Locate the cells, classifying each as a parasitized RBC, an uninfected RBC, or a WBC.
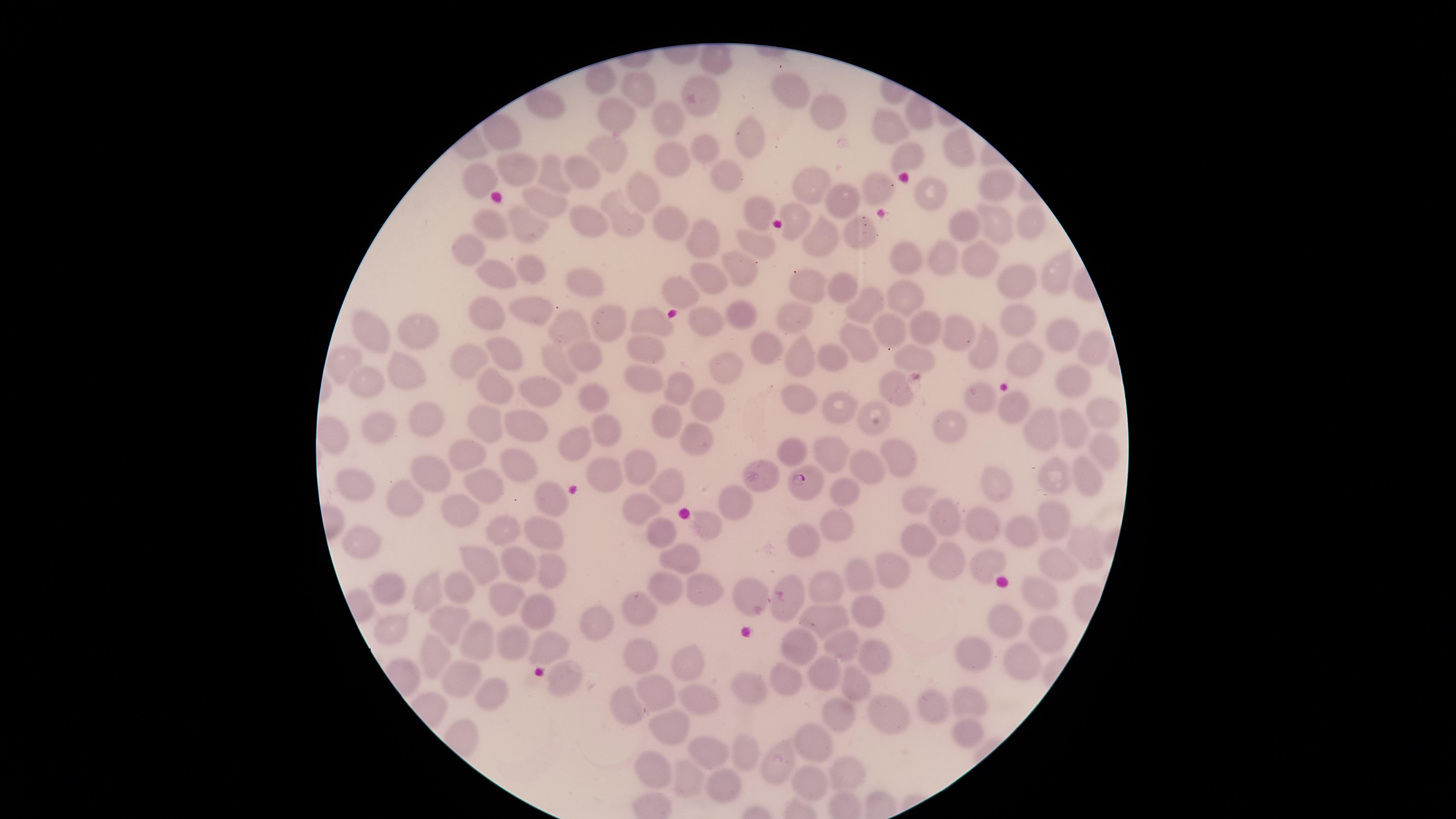
Approximate marker points, in pixels from the top-left corner.
Parasitized RBCs: (x=807, y=483).
Uninfected RBCs: (x=713, y=52), (x=605, y=78), (x=638, y=85), (x=795, y=90), (x=703, y=100), (x=547, y=107), (x=824, y=114), (x=913, y=114), (x=620, y=115), (x=673, y=118), (x=890, y=129), (x=748, y=133), (x=504, y=135), (x=705, y=145), (x=960, y=146), (x=603, y=151), (x=913, y=154), (x=671, y=158), (x=582, y=168), (x=726, y=172), (x=552, y=173), (x=511, y=177), (x=809, y=180), (x=999, y=184), (x=477, y=185), (x=639, y=185), (x=880, y=188), (x=929, y=197), (x=544, y=198), (x=843, y=199), (x=758, y=204), (x=622, y=215), (x=489, y=222), (x=598, y=222), (x=667, y=222), (x=1026, y=224), (x=994, y=225), (x=794, y=226), (x=855, y=226), (x=971, y=226), (x=530, y=227), (x=700, y=235), (x=754, y=236), (x=814, y=238), (x=471, y=248), (x=941, y=251), (x=898, y=255), (x=975, y=256), (x=742, y=266), (x=525, y=269), (x=494, y=270), (x=1054, y=270), (x=707, y=275), (x=1007, y=281), (x=581, y=284), (x=674, y=285), (x=807, y=285), (x=841, y=288), (x=909, y=294), (x=869, y=306), (x=526, y=309), (x=746, y=312), (x=487, y=313), (x=797, y=314), (x=704, y=316), (x=649, y=317), (x=1013, y=317), (x=606, y=321), (x=563, y=324), (x=429, y=327), (x=920, y=327), (x=959, y=329), (x=1060, y=329), (x=375, y=332), (x=892, y=332), (x=1089, y=341), (x=862, y=342), (x=643, y=345), (x=761, y=345), (x=987, y=351), (x=501, y=353), (x=583, y=355), (x=913, y=355), (x=806, y=356), (x=830, y=356), (x=339, y=360), (x=1025, y=360), (x=563, y=363), (x=476, y=365), (x=725, y=365), (x=410, y=372), (x=646, y=377), (x=1075, y=377), (x=371, y=378), (x=543, y=387), (x=496, y=389), (x=674, y=389), (x=899, y=389), (x=589, y=392), (x=981, y=395), (x=800, y=397), (x=706, y=401), (x=1012, y=407), (x=839, y=411), (x=1101, y=413), (x=421, y=418), (x=672, y=418), (x=481, y=419), (x=866, y=421), (x=951, y=421), (x=516, y=424), (x=1075, y=426), (x=601, y=428), (x=381, y=430), (x=1048, y=430), (x=335, y=436), (x=696, y=436), (x=459, y=447), (x=574, y=447), (x=836, y=449), (x=1106, y=450), (x=790, y=452), (x=895, y=454), (x=518, y=466), (x=639, y=467), (x=425, y=470), (x=607, y=471), (x=1089, y=472), (x=879, y=473), (x=1052, y=476), (x=761, y=480), (x=993, y=480), (x=484, y=483), (x=361, y=486), (x=667, y=486), (x=843, y=494), (x=405, y=497), (x=548, y=497), (x=919, y=499), (x=736, y=503), (x=642, y=506), (x=459, y=509), (x=941, y=516), (x=1053, y=516), (x=710, y=525), (x=840, y=526), (x=981, y=526), (x=657, y=527), (x=547, y=530), (x=504, y=532), (x=362, y=536), (x=1021, y=536), (x=916, y=540), (x=1086, y=545), (x=679, y=554), (x=949, y=557), (x=988, y=562), (x=479, y=565), (x=516, y=566), (x=1060, y=568), (x=889, y=569), (x=551, y=572), (x=864, y=577), (x=669, y=586), (x=828, y=586), (x=434, y=588), (x=473, y=589), (x=1036, y=589), (x=702, y=590), (x=386, y=592), (x=505, y=596), (x=753, y=600), (x=862, y=608), (x=641, y=612), (x=535, y=613), (x=825, y=613), (x=448, y=621), (x=596, y=623), (x=1004, y=624), (x=1045, y=631), (x=513, y=637), (x=477, y=639), (x=837, y=642), (x=546, y=644), (x=799, y=646), (x=641, y=653), (x=1020, y=653), (x=873, y=655), (x=433, y=656), (x=976, y=657), (x=685, y=661), (x=824, y=671), (x=452, y=672), (x=782, y=679), (x=563, y=680), (x=658, y=689), (x=747, y=689), (x=853, y=689), (x=482, y=691), (x=696, y=695), (x=968, y=696), (x=926, y=706), (x=625, y=709), (x=842, y=713), (x=878, y=715), (x=672, y=726), (x=963, y=727), (x=816, y=738), (x=746, y=747), (x=704, y=751), (x=646, y=761), (x=786, y=765), (x=844, y=770), (x=686, y=774), (x=816, y=781), (x=721, y=782).
No WBCs identified.

{
  "image_size": "1456×819 pixels",
  "field_of_view": "single",
  "stain": "Giemsa",
  "preparation": "thin blood smear",
  "capture": "smartphone photograph through the microscope eyepiece",
  "species": "Plasmodium falciparum",
  "visible_region": "circular"
}